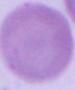

Summary:
  - Modality: micrograph
  - Identification: erythrocyte
  - Magnification: 1000x